Identify the cell.
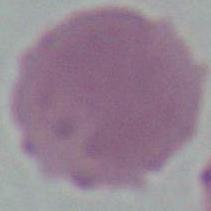

An erythrocyte.

Micrograph. 1000x magnification.